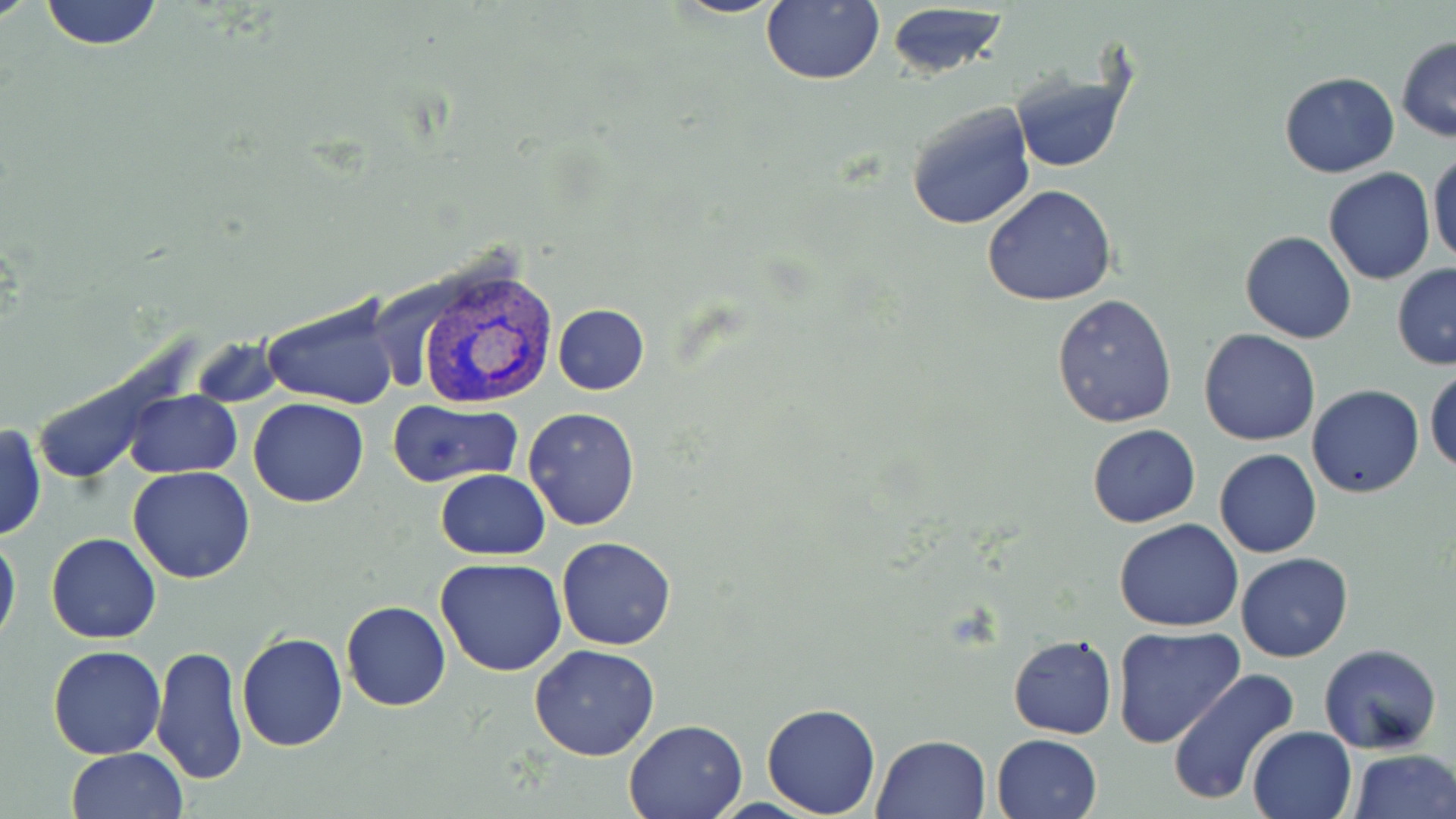

slide-level diagnosis = Plasmodium vivax
magnification = 1000x
field of view = one of a larger specimen
modality = optical microscopy
image size = 1456×819 pixels
uninfected red blood cell locations = approximate bounding boxes as [x1, y1, x2, y2] in pixels: [39, 0, 164, 50], [761, 0, 884, 86], [885, 4, 1008, 79], [1395, 36, 1456, 142], [1010, 62, 1132, 174], [1279, 72, 1399, 178], [905, 101, 1036, 232], [1428, 149, 1456, 269], [1323, 168, 1436, 285], [981, 185, 1118, 306], [1239, 231, 1357, 344], [1391, 264, 1456, 370], [1052, 293, 1179, 429], [263, 297, 397, 410], [552, 304, 650, 395], [1198, 330, 1321, 446], [192, 338, 284, 408], [1424, 366, 1456, 475], [1306, 385, 1425, 498], [125, 390, 240, 477], [248, 397, 369, 507], [386, 400, 523, 487], [523, 406, 640, 532], [1, 422, 46, 543], [1087, 424, 1200, 528], [1214, 449, 1322, 558], [128, 466, 256, 584], [435, 469, 550, 560], [1115, 519, 1244, 633], [0, 531, 21, 648], [45, 532, 162, 643], [556, 536, 677, 652], [1236, 552, 1353, 663], [435, 558, 568, 677], [342, 601, 450, 712], [1114, 627, 1245, 749], [238, 632, 349, 751], [1007, 634, 1117, 739], [1317, 642, 1442, 753], [150, 645, 247, 785], [529, 645, 660, 762], [46, 646, 166, 760], [1167, 669, 1299, 808], [761, 703, 883, 818], [623, 718, 749, 818], [1246, 725, 1357, 819], [872, 733, 990, 818], [991, 734, 1102, 819], [66, 748, 187, 819], [1346, 748, 1454, 819]
stain = May-Grünwald-Giemsa
Plasmodium vivax-infected red blood cell locations = approximate bounding boxes as [x1, y1, x2, y2] in pixels: [412, 266, 559, 409]
preparation = thin blood smear